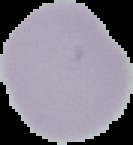
image size = 133×145 pixels
preparation = thin blood film
image type = segmented cell region with the area outside set to black
result = no Plasmodium parasites detected